Assess this cell for malaria.
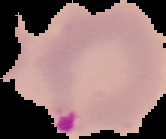
Parasitized.

Image is 166×139 pixels. Cell region segmented out of the field of view; the surrounding area is masked to black. From a thin blood smear.